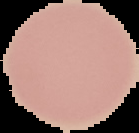

Summary:
  - Image size: 139×133 pixels
  - Image type: segmented cell region on a black background
  - Malaria status: uninfected
  - Preparation: thin blood film